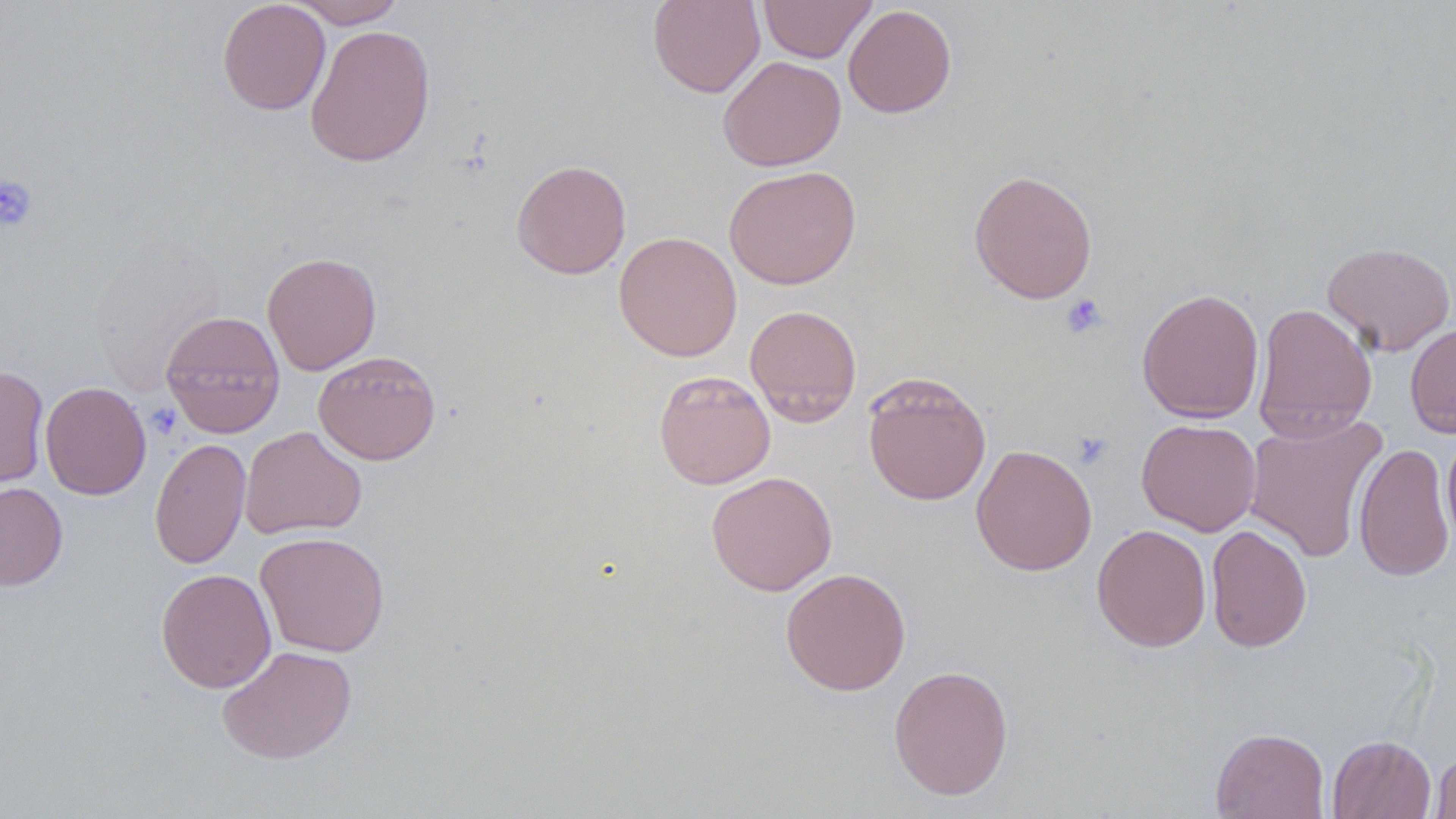 Approximate bounding boxes as (x1, y1, x2, y2) in pixels. Platelet locations: (0, 176, 38, 231), (1059, 294, 1107, 339), (1072, 433, 1114, 471). Uninfected red blood cell locations: (217, 0, 331, 115), (289, 0, 406, 28), (648, 0, 765, 98), (758, 0, 876, 63), (843, 4, 957, 118), (304, 24, 436, 167), (718, 55, 846, 171), (511, 159, 631, 279), (723, 165, 861, 290), (968, 169, 1098, 304), (613, 231, 742, 361), (1322, 241, 1455, 356), (262, 251, 382, 375), (1136, 288, 1264, 423), (1252, 303, 1378, 442), (745, 304, 862, 425), (160, 310, 286, 438), (1405, 322, 1456, 438), (313, 350, 441, 465), (0, 364, 49, 488), (653, 370, 776, 489), (862, 372, 992, 506), (40, 381, 151, 500), (1243, 414, 1388, 562), (1136, 418, 1261, 536), (240, 426, 367, 540), (1442, 427, 1456, 546), (149, 437, 251, 570), (1353, 442, 1455, 582), (971, 444, 1097, 576), (706, 471, 837, 596), (0, 482, 68, 591), (1092, 523, 1211, 652), (1206, 524, 1312, 653), (255, 531, 390, 657), (780, 567, 911, 695), (155, 568, 276, 693), (217, 645, 357, 764), (889, 664, 1014, 800), (1210, 727, 1330, 819), (1327, 735, 1436, 819), (1429, 752, 1456, 818). Slide-level diagnosis: no evidence of blood parasites. May-Grünwald-Giemsa-stained preparation. Captured at 1000x magnification. Optical microscopy. Image is 1456×819 pixels. Thin blood smear. Single field of view.